Outline each blood parasite and name the species.
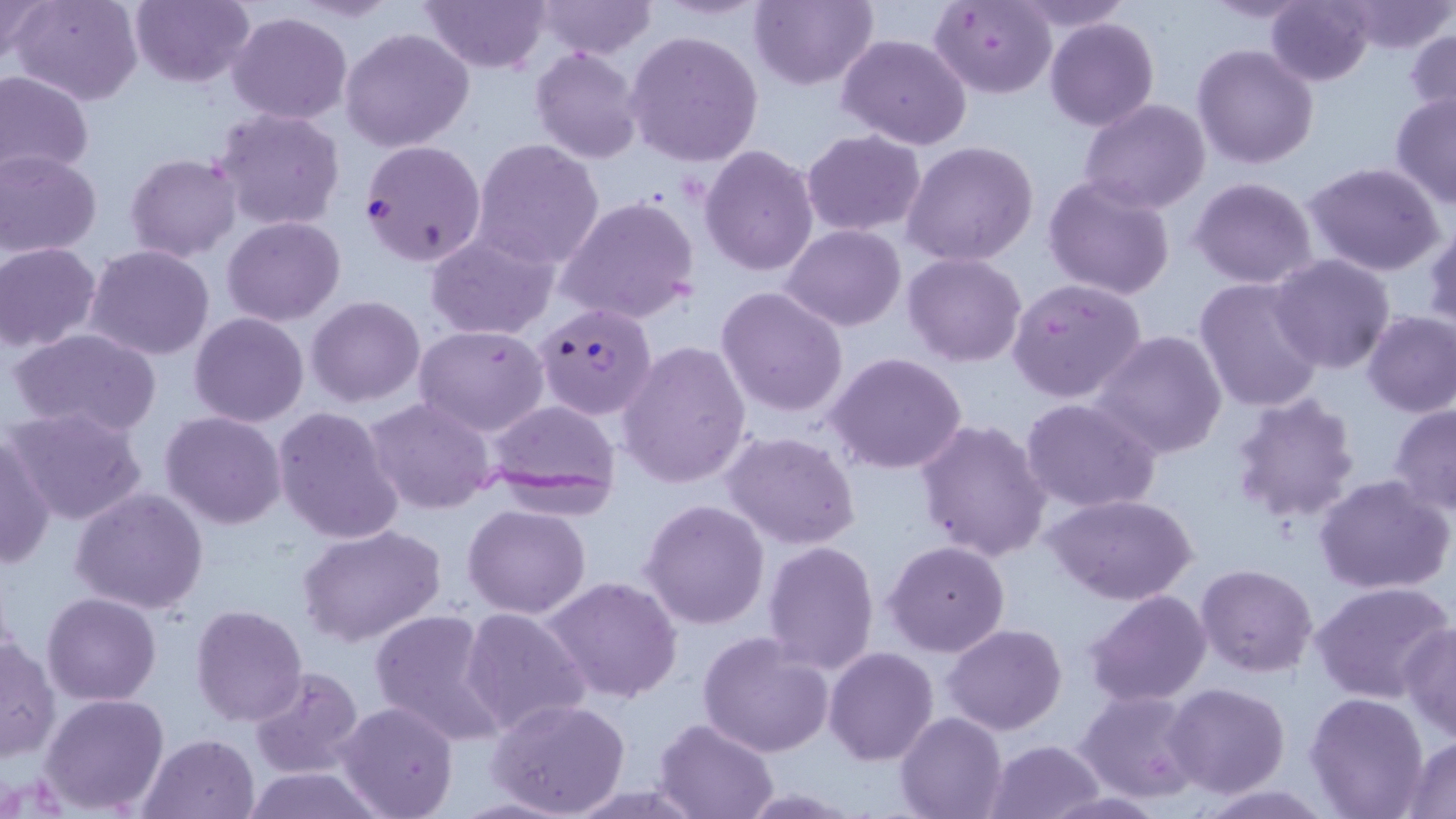
Approximate bounding boxes as [x1, y1, x2, y2] in pixels.
Plasmodium falciparum-infected red blood cells: [360, 140, 486, 266], [534, 303, 656, 420].
No Plasmodium ovale, Plasmodium malariae, Plasmodium vivax, Babesia divergens, or Trypanosoma brucei observed.

Summary:
  - Uninfected red blood cell locations: [0, 0, 52, 65], [10, 0, 143, 106], [130, 0, 256, 88], [420, 0, 551, 72], [536, 0, 659, 58], [750, 0, 876, 91], [1010, 0, 1133, 31], [1197, 0, 1315, 22], [1266, 0, 1375, 86], [929, 1, 1057, 98], [1341, 1, 1453, 55], [227, 10, 352, 124], [1046, 17, 1159, 131], [1405, 27, 1456, 129], [340, 28, 474, 152], [624, 30, 765, 167], [836, 35, 971, 151], [1193, 43, 1319, 169], [531, 47, 644, 164], [0, 69, 94, 180], [1390, 89, 1456, 211], [1079, 98, 1211, 214], [212, 106, 345, 231], [802, 130, 925, 237], [472, 140, 604, 267], [902, 140, 1039, 267], [700, 145, 819, 277], [0, 150, 102, 257], [124, 153, 241, 261], [1303, 163, 1446, 277], [1044, 173, 1177, 300], [1190, 177, 1319, 289], [556, 195, 700, 326], [222, 215, 346, 325], [1424, 221, 1456, 333], [782, 224, 907, 330], [425, 231, 558, 339], [0, 244, 101, 353], [86, 245, 215, 362], [903, 253, 1028, 367], [1270, 254, 1394, 373], [1194, 277, 1326, 413], [1007, 278, 1146, 403], [716, 287, 849, 418], [306, 296, 426, 407], [1362, 309, 1456, 417], [189, 312, 308, 426], [414, 323, 550, 437], [6, 326, 163, 440], [1092, 330, 1229, 459], [616, 341, 751, 489], [825, 352, 969, 475], [1229, 391, 1360, 525], [364, 397, 497, 515], [1021, 397, 1163, 515], [484, 401, 621, 508], [1388, 402, 1456, 515], [272, 405, 404, 544], [6, 406, 149, 528], [160, 410, 287, 530], [915, 419, 1053, 562], [0, 429, 54, 571], [719, 430, 862, 550], [1314, 474, 1453, 596], [69, 487, 209, 615], [1045, 493, 1197, 606], [641, 498, 769, 630], [464, 503, 591, 618], [297, 524, 447, 647], [883, 539, 1010, 658], [761, 541, 880, 675], [1196, 564, 1319, 678], [545, 576, 682, 704], [1310, 580, 1454, 704], [1084, 589, 1213, 708], [43, 593, 163, 706], [190, 605, 308, 728], [460, 606, 590, 738], [369, 609, 506, 745], [944, 623, 1067, 734], [1400, 623, 1456, 741], [697, 631, 838, 758], [0, 637, 58, 762], [824, 647, 940, 766], [248, 666, 363, 779], [1165, 682, 1291, 800], [1077, 691, 1205, 803], [40, 692, 168, 815], [1306, 692, 1432, 819], [487, 698, 632, 819], [334, 700, 459, 818], [896, 711, 1007, 819], [653, 717, 779, 819], [137, 732, 259, 818], [1401, 735, 1456, 817], [984, 738, 1106, 818], [241, 765, 384, 819], [1195, 783, 1334, 818]
  - Slide-level diagnosis: Plasmodium falciparum
  - Stain: May-Grünwald-Giemsa
  - Image size: 1456×819 pixels
  - Modality: light microscopy
  - Preparation: thin blood smear
  - Magnification: 1000x
  - Field of view: one of a larger specimen